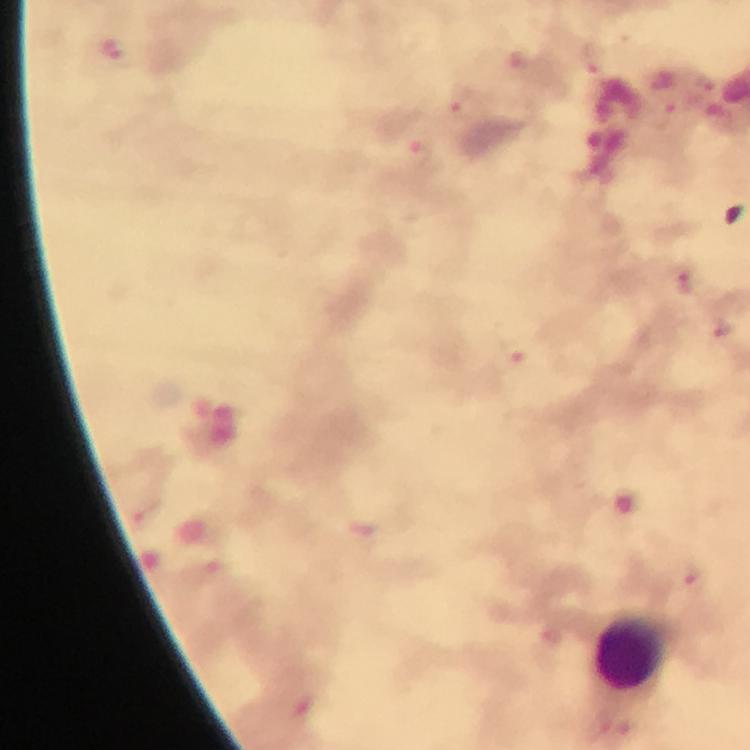 Approximate centers as {x, y} in pixels. Plasmodium parasite locations: {591, 59}, {466, 102}, {683, 283}, {515, 353}. Leukocyte locations: {634, 652}. At 100x magnification. A crop from one field of view. Giemsa-stained preparation. From a diagnostic examination for malaria. Immersion oil applied. Thick blood smear. Image is 750×750 pixels. Photographed through the microscope with a smartphone camera.